State which parasite is depicted.
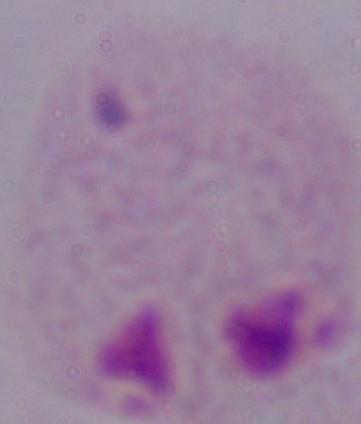

This is a trichomonad.

Summary:
  - Magnification: 1000x
  - Modality: photomicrograph